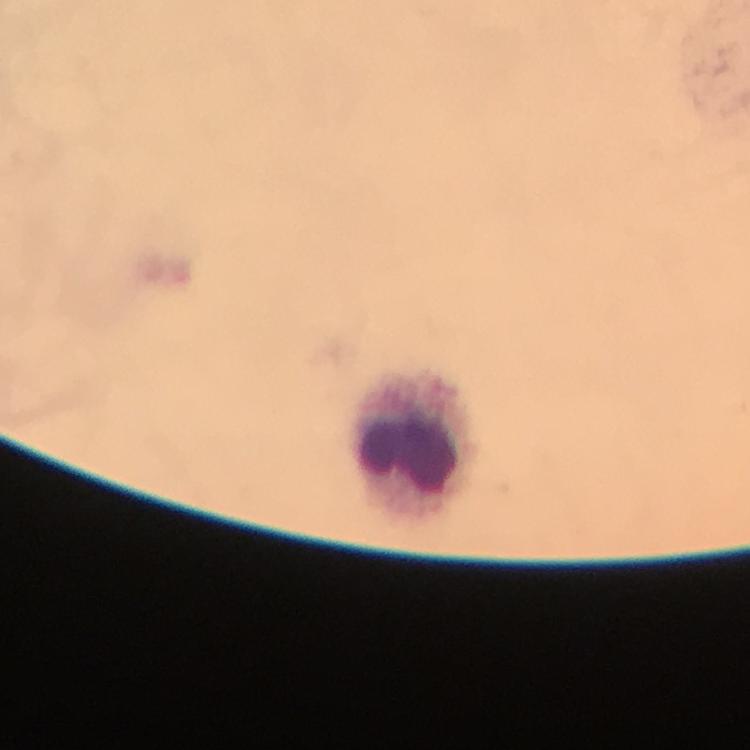
Approximate centers as {x, y} in pixels.
Summary:
  - Leukocyte locations: {413, 446}
  - Capture: smartphone photograph through a microscope
  - Immersion oil: applied
  - Cropped from: one field of view
  - Stain: Giemsa
  - Magnification: 100x
  - Preparation: thick blood film
  - Plasmodium parasites: none seen
  - Context: from a diagnostic examination for malaria
  - Image size: 750×750 pixels